Point out every Plasmodium parasite.
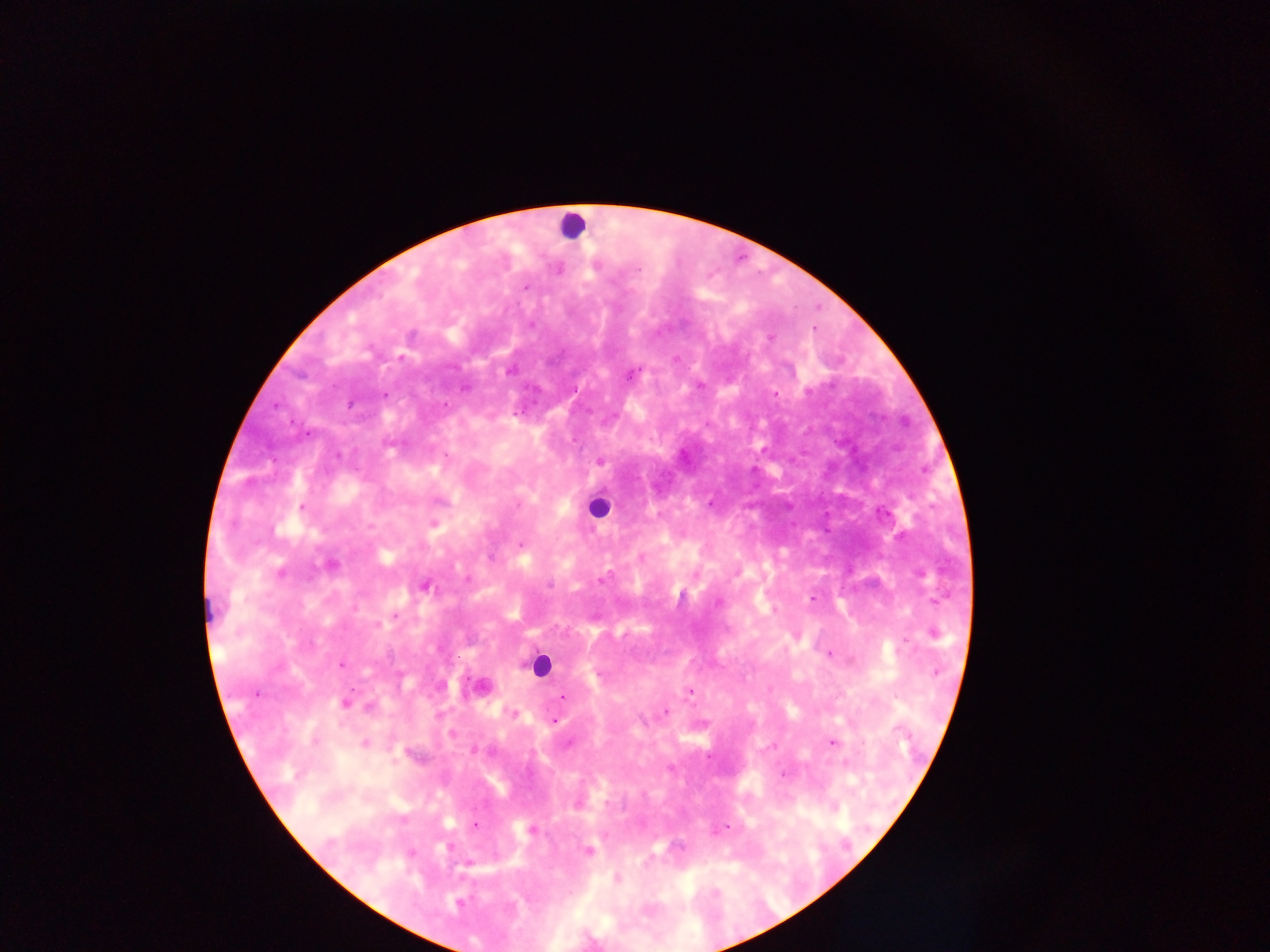
Approximate centers as x y in pixels.
Plasmodium parasites: 557 268; 526 287; 813 329; 770 337; 630 374; 699 385; 775 392; 600 460; 301 507; 433 523; 520 544; 640 557; 330 565; 920 573; 601 580; 424 586; 811 598; 717 602; 933 633; 829 653; 341 665; 934 672; 480 687; 689 692; 562 696; 344 702; 368 706; 666 710; 513 714; 553 720; 452 734; 830 741; 364 742; 474 825; 721 828; 531 830; 588 851; 616 878; 458 903.

Leukocyte locations: 571 226; 599 507; 213 609; 540 664. Collected in Ghana. Image is 1270×952 pixels. Thick blood smear. One field of view. Photographed through a microscope with a mobile-phone camera.